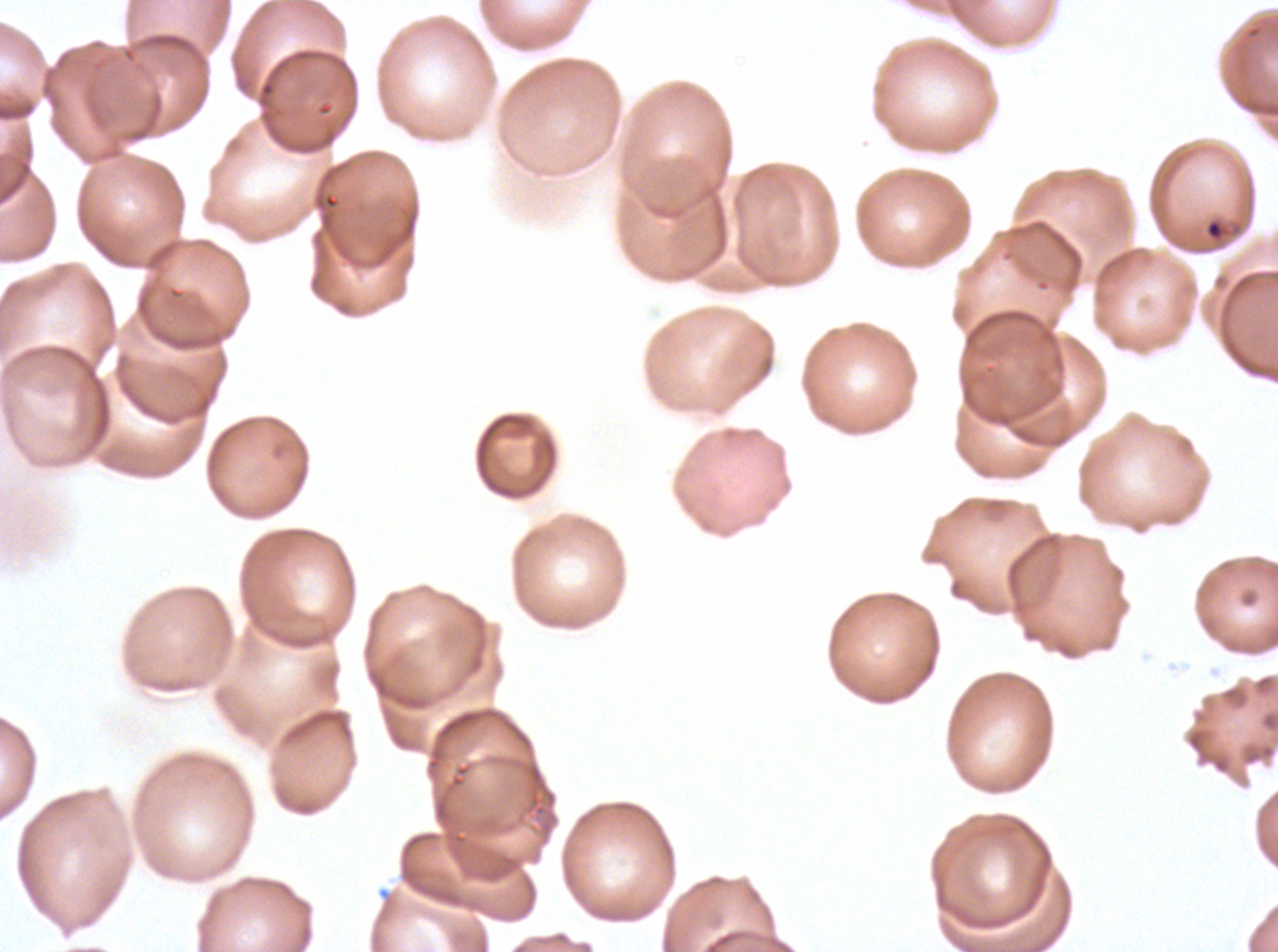

Approximate bounding rectangles given as corner coordinates in pixels from the top-left. Debris locations: (x1=1203, y1=217, x2=1241, y2=244). Giemsa-stained preparation. Thin blood film. One sub-image of a larger composite. Image is 1278×952 pixels. Ex-vivo P. falciparum culture from a patient in The Gambia, grown for 24 to 48 hours.